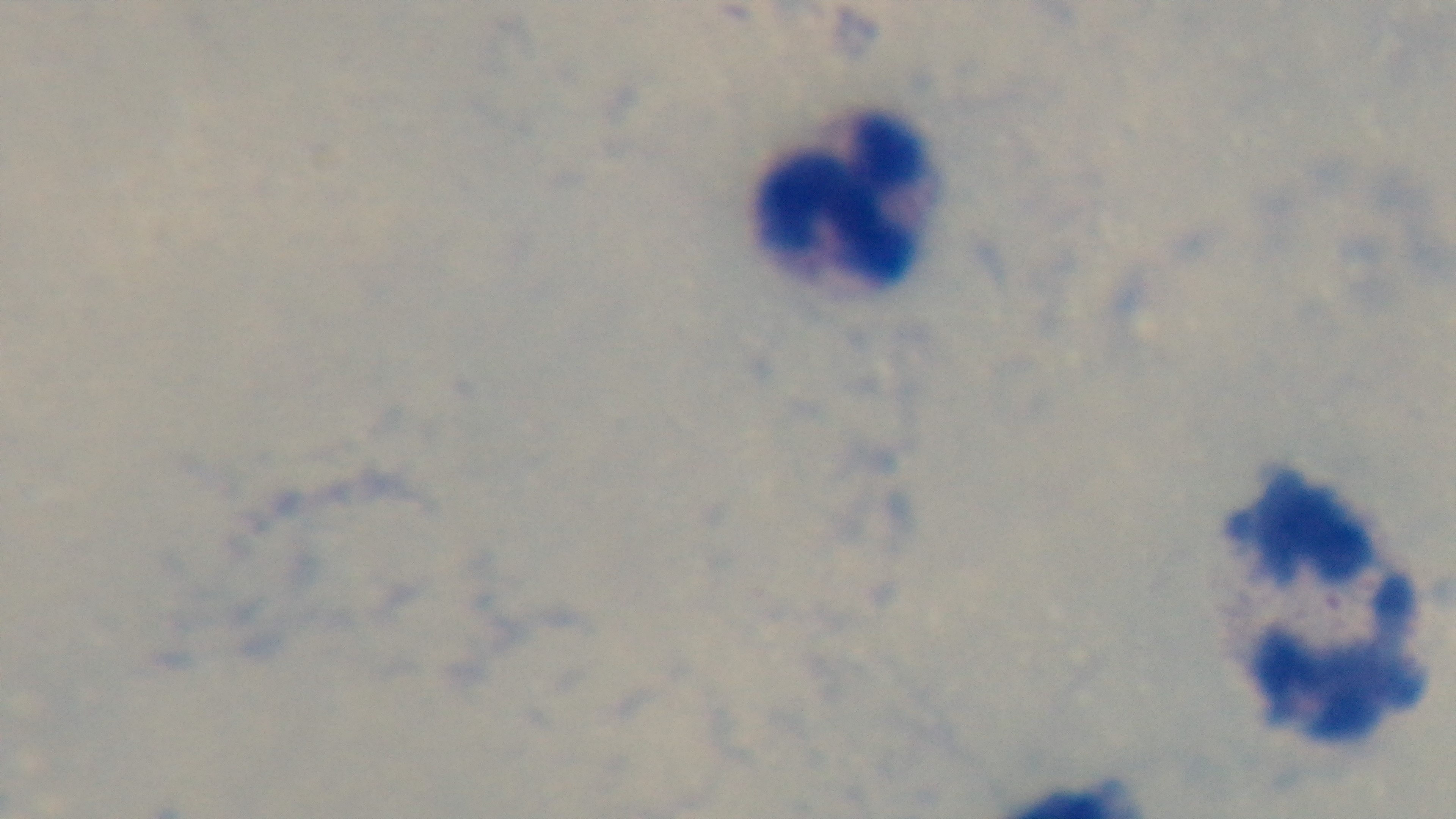

Summary:
  - Preparation: thick
  - Field of view: single
  - Objective: 100x oil immersion
  - Capture: mounted 4K digital camera
  - Stain: Giemsa
  - Malaria status: uninfected
  - Modality: light microscopy